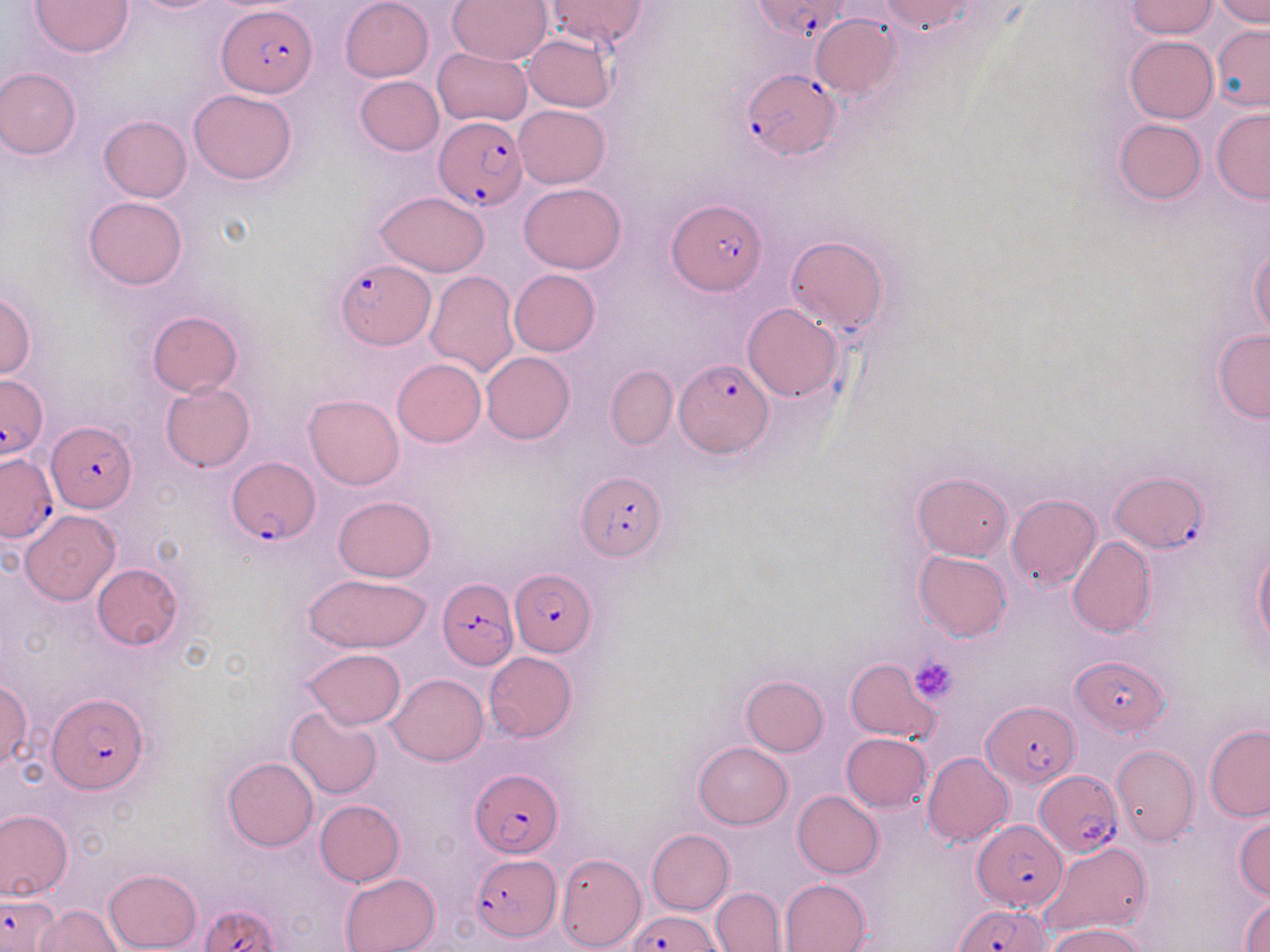
Approximate bounding boxes as named x1/y1/x2/y2 corners in pixels. Uninfected red blood cell locations: (x1=31, y1=0, x2=134, y2=57), (x1=340, y1=0, x2=433, y2=83), (x1=447, y1=0, x2=554, y2=67), (x1=1213, y1=0, x2=1270, y2=26), (x1=548, y1=1, x2=645, y2=48), (x1=1125, y1=1, x2=1219, y2=38), (x1=808, y1=11, x2=902, y2=99), (x1=1211, y1=25, x2=1270, y2=110), (x1=522, y1=34, x2=616, y2=113), (x1=1124, y1=35, x2=1219, y2=123), (x1=432, y1=48, x2=532, y2=126), (x1=0, y1=67, x2=81, y2=160), (x1=355, y1=76, x2=444, y2=156), (x1=188, y1=88, x2=298, y2=184), (x1=515, y1=105, x2=609, y2=189), (x1=1211, y1=108, x2=1270, y2=203), (x1=100, y1=116, x2=191, y2=201), (x1=1114, y1=118, x2=1206, y2=203), (x1=519, y1=181, x2=626, y2=274), (x1=374, y1=190, x2=490, y2=277), (x1=84, y1=196, x2=188, y2=289), (x1=785, y1=236, x2=889, y2=335), (x1=1249, y1=246, x2=1270, y2=338), (x1=508, y1=269, x2=601, y2=356), (x1=424, y1=270, x2=520, y2=377), (x1=0, y1=287, x2=36, y2=381), (x1=743, y1=303, x2=844, y2=401), (x1=146, y1=310, x2=242, y2=397), (x1=1214, y1=330, x2=1270, y2=423), (x1=481, y1=351, x2=574, y2=444), (x1=392, y1=358, x2=486, y2=447), (x1=606, y1=365, x2=677, y2=449), (x1=161, y1=382, x2=254, y2=472), (x1=304, y1=393, x2=404, y2=490), (x1=913, y1=472, x2=1012, y2=559), (x1=334, y1=495, x2=436, y2=582), (x1=1006, y1=495, x2=1101, y2=591), (x1=20, y1=511, x2=121, y2=606), (x1=1067, y1=536, x2=1157, y2=638), (x1=1254, y1=545, x2=1270, y2=650), (x1=914, y1=550, x2=1012, y2=641), (x1=92, y1=563, x2=184, y2=650), (x1=304, y1=574, x2=432, y2=653), (x1=302, y1=648, x2=407, y2=728), (x1=483, y1=651, x2=575, y2=741), (x1=845, y1=657, x2=940, y2=742), (x1=389, y1=673, x2=488, y2=766), (x1=740, y1=674, x2=828, y2=755), (x1=0, y1=678, x2=33, y2=771), (x1=285, y1=706, x2=383, y2=799), (x1=1205, y1=724, x2=1270, y2=819), (x1=841, y1=732, x2=931, y2=812), (x1=693, y1=742, x2=792, y2=829), (x1=1112, y1=745, x2=1199, y2=847), (x1=922, y1=752, x2=1014, y2=845), (x1=222, y1=757, x2=318, y2=852), (x1=792, y1=791, x2=883, y2=877), (x1=315, y1=799, x2=404, y2=886), (x1=0, y1=810, x2=72, y2=901), (x1=1233, y1=814, x2=1270, y2=900), (x1=645, y1=829, x2=734, y2=915), (x1=1043, y1=841, x2=1152, y2=937), (x1=555, y1=853, x2=645, y2=951), (x1=104, y1=868, x2=202, y2=951), (x1=339, y1=872, x2=440, y2=952), (x1=780, y1=878, x2=871, y2=952), (x1=711, y1=887, x2=785, y2=951), (x1=1240, y1=893, x2=1270, y2=950), (x1=34, y1=904, x2=122, y2=951), (x1=1047, y1=924, x2=1147, y2=952). Platelet locations: (x1=909, y1=656, x2=957, y2=702). Plasmodium falciparum-infected red blood cell locations: (x1=752, y1=0, x2=852, y2=44), (x1=219, y1=6, x2=318, y2=97), (x1=740, y1=70, x2=840, y2=160), (x1=432, y1=116, x2=528, y2=211), (x1=668, y1=200, x2=766, y2=293), (x1=335, y1=259, x2=434, y2=349), (x1=675, y1=359, x2=773, y2=456), (x1=0, y1=375, x2=49, y2=459), (x1=45, y1=423, x2=137, y2=512), (x1=0, y1=453, x2=57, y2=541), (x1=226, y1=457, x2=319, y2=544), (x1=1109, y1=470, x2=1206, y2=553), (x1=576, y1=473, x2=666, y2=562), (x1=511, y1=569, x2=596, y2=657), (x1=438, y1=576, x2=519, y2=670), (x1=1073, y1=655, x2=1167, y2=735), (x1=46, y1=692, x2=148, y2=793), (x1=983, y1=700, x2=1078, y2=788), (x1=470, y1=769, x2=563, y2=857), (x1=1034, y1=770, x2=1122, y2=857), (x1=972, y1=819, x2=1069, y2=911), (x1=469, y1=855, x2=559, y2=941), (x1=0, y1=893, x2=59, y2=950), (x1=201, y1=903, x2=280, y2=952), (x1=955, y1=905, x2=1049, y2=952), (x1=630, y1=910, x2=722, y2=951). Slide-level diagnosis: Plasmodium falciparum. Single field of view. Captured at 1000x magnification. Thin blood smear. Image is 1270×952 pixels. May-Grünwald-Giemsa-stained preparation. Optical microscopy.